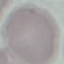
Summary:
  - Malaria status: uninfected
  - Preparation: thin blood film
  - Stain: Giemsa
  - Capture: smartphone camera at the microscope eyepiece
  - Image type: cell patch, automatically extracted from a larger field of view and resized to 64 × 64 pixels